State the blood parasite species.
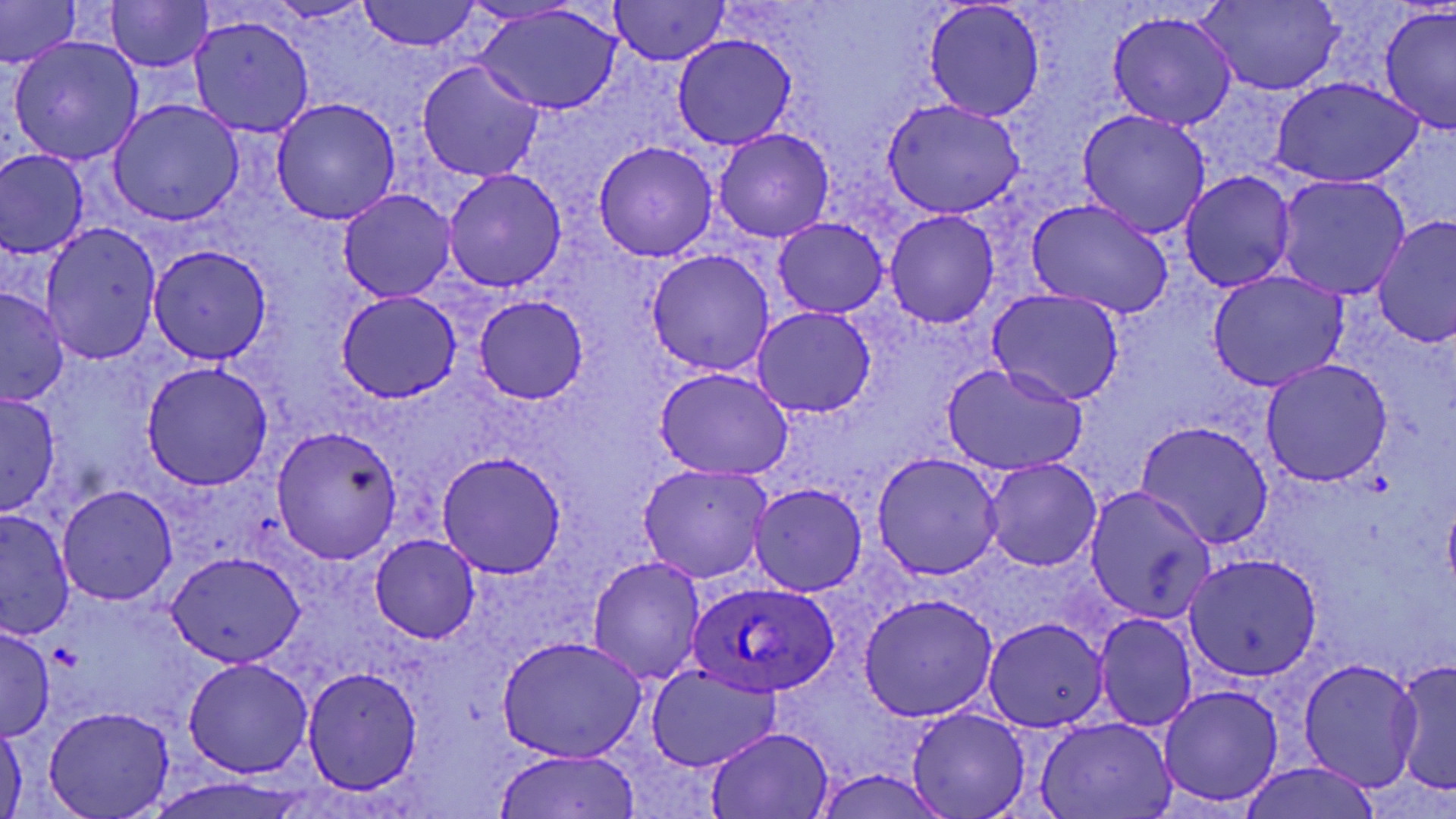

Plasmodium ovale.

Approximate bounding boxes as named x1/y1/x2/y2 corners in pixels. Plasmodium ovale-infected red blood cell locations: (x1=689, y1=578, x2=838, y2=697). Uninfected red blood cell locations: (x1=103, y1=0, x2=217, y2=72), (x1=359, y1=0, x2=482, y2=53), (x1=920, y1=0, x2=1048, y2=123), (x1=1194, y1=0, x2=1345, y2=96), (x1=608, y1=1, x2=732, y2=64), (x1=0, y1=3, x2=84, y2=69), (x1=474, y1=3, x2=627, y2=117), (x1=1378, y1=5, x2=1455, y2=137), (x1=1106, y1=9, x2=1238, y2=130), (x1=185, y1=14, x2=315, y2=136), (x1=6, y1=34, x2=146, y2=167), (x1=671, y1=34, x2=799, y2=151), (x1=416, y1=60, x2=548, y2=184), (x1=1268, y1=75, x2=1427, y2=189), (x1=880, y1=95, x2=1031, y2=220), (x1=270, y1=97, x2=402, y2=225), (x1=106, y1=98, x2=243, y2=227), (x1=1075, y1=107, x2=1211, y2=240), (x1=713, y1=128, x2=835, y2=243), (x1=592, y1=140, x2=722, y2=262), (x1=0, y1=148, x2=90, y2=261), (x1=442, y1=169, x2=567, y2=293), (x1=1179, y1=170, x2=1298, y2=293), (x1=1271, y1=173, x2=1411, y2=300), (x1=337, y1=188, x2=457, y2=304), (x1=1023, y1=194, x2=1176, y2=319), (x1=882, y1=208, x2=1000, y2=329), (x1=1375, y1=214, x2=1455, y2=349), (x1=770, y1=216, x2=889, y2=317), (x1=39, y1=223, x2=161, y2=365), (x1=147, y1=246, x2=271, y2=366), (x1=643, y1=249, x2=774, y2=377), (x1=1205, y1=269, x2=1351, y2=392), (x1=0, y1=285, x2=71, y2=407), (x1=986, y1=289, x2=1128, y2=406), (x1=333, y1=291, x2=463, y2=404), (x1=472, y1=294, x2=590, y2=403), (x1=752, y1=307, x2=877, y2=418), (x1=1257, y1=356, x2=1394, y2=486), (x1=139, y1=359, x2=278, y2=489), (x1=939, y1=361, x2=1088, y2=478), (x1=654, y1=366, x2=794, y2=482), (x1=0, y1=390, x2=62, y2=518), (x1=1135, y1=420, x2=1275, y2=550), (x1=271, y1=427, x2=404, y2=564), (x1=435, y1=450, x2=570, y2=577), (x1=870, y1=450, x2=1006, y2=581), (x1=981, y1=457, x2=1101, y2=571), (x1=635, y1=461, x2=773, y2=585), (x1=749, y1=483, x2=868, y2=598), (x1=58, y1=484, x2=177, y2=604), (x1=1082, y1=486, x2=1215, y2=626), (x1=0, y1=507, x2=72, y2=642), (x1=368, y1=535, x2=479, y2=643), (x1=165, y1=550, x2=305, y2=670), (x1=1180, y1=553, x2=1322, y2=684), (x1=587, y1=555, x2=706, y2=682), (x1=857, y1=591, x2=999, y2=722), (x1=1092, y1=612, x2=1200, y2=731), (x1=982, y1=617, x2=1107, y2=734), (x1=0, y1=626, x2=54, y2=740), (x1=494, y1=634, x2=649, y2=765), (x1=181, y1=655, x2=314, y2=778), (x1=1296, y1=657, x2=1426, y2=793), (x1=1391, y1=659, x2=1455, y2=797), (x1=645, y1=663, x2=782, y2=772), (x1=300, y1=666, x2=425, y2=794), (x1=1155, y1=682, x2=1286, y2=813), (x1=42, y1=704, x2=175, y2=819), (x1=905, y1=705, x2=1032, y2=819), (x1=1035, y1=716, x2=1179, y2=819), (x1=0, y1=717, x2=26, y2=817), (x1=705, y1=727, x2=834, y2=818), (x1=493, y1=749, x2=641, y2=819). Image is 1456×819 pixels. Single field of view. Light microscopy. Thin blood smear. May-Grünwald-Giemsa stain. Captured at 1000x magnification.